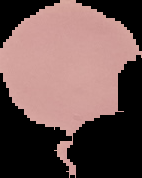
From a thin blood film. Segmented cell region on a black background. Image is 142×178 pixels. Malaria status: uninfected.